Classify this cell by malaria status.
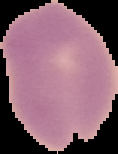
It is uninfected.

image size = 118×154 pixels
image type = segmented cell region with the area outside set to black
preparation = thin blood film